Identify the parasite.
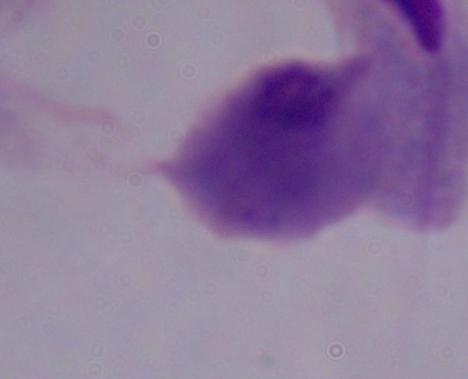

This is a trichomonad.

magnification: 1000x
modality: photomicrograph